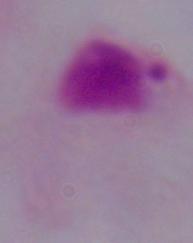 1000x magnification. Photomicrograph. A trichomonad is shown.